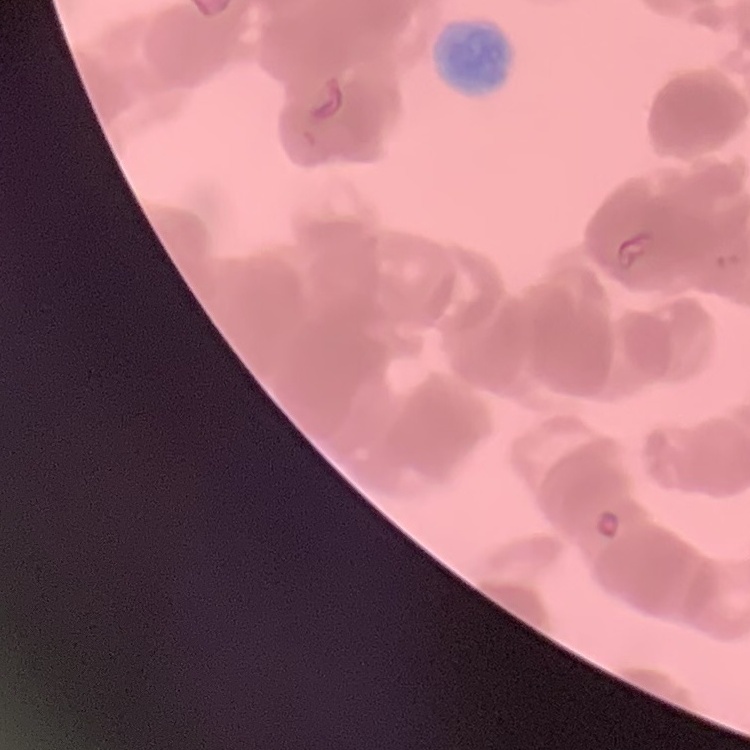

The erythrocytes exhibit rouleaux formation. Thin peripheral smear. Field's or Giemsa stain. Square crop of a larger photomicrograph.